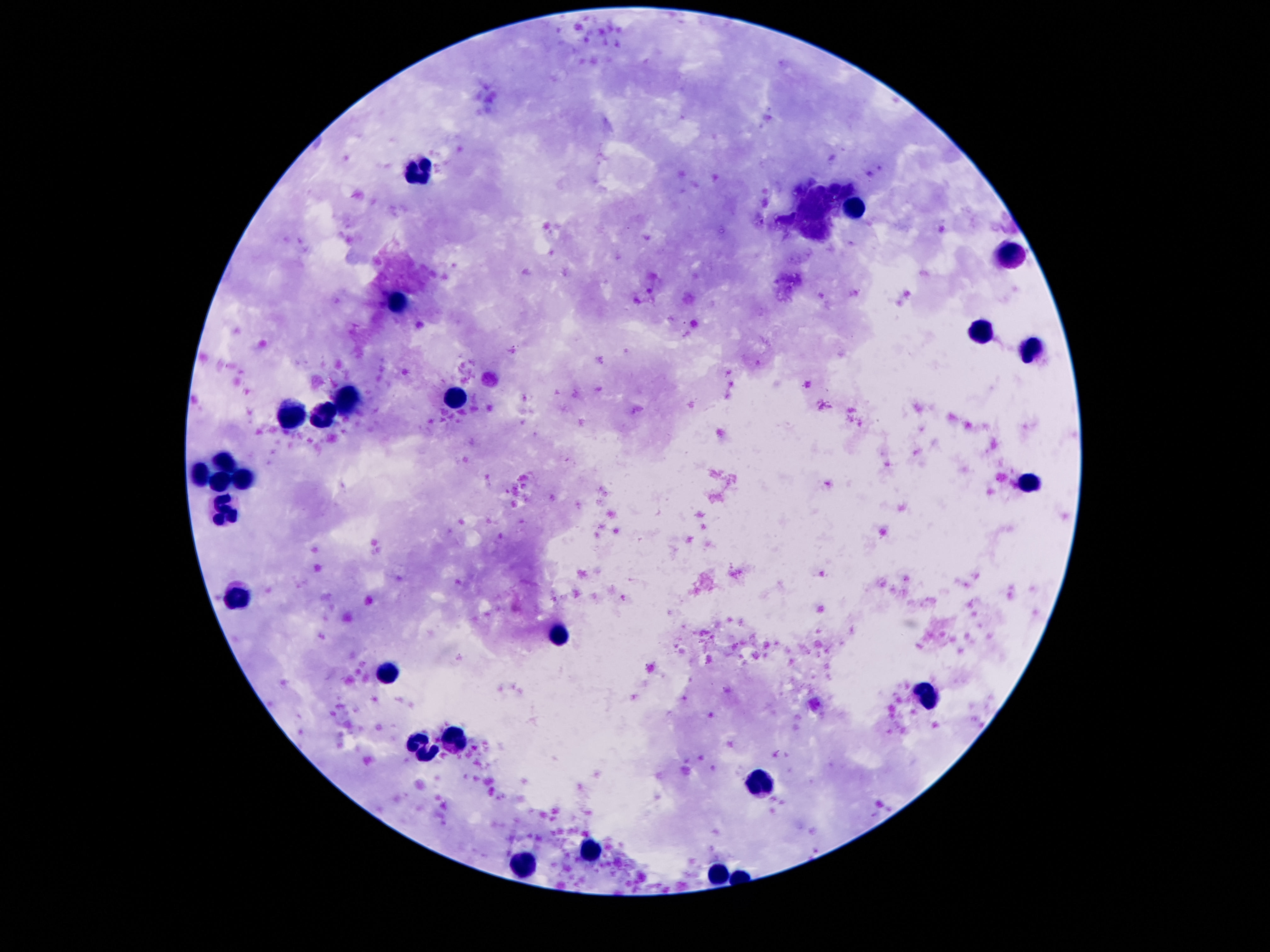

Approximate centers as {x, y} in pixels. Leukocyte locations: {422, 171}, {856, 208}, {1006, 255}, {398, 300}, {982, 330}, {1030, 351}, {458, 395}, {347, 397}, {290, 416}, {323, 416}, {228, 460}, {199, 474}, {221, 477}, {241, 479}, {1030, 485}, {226, 510}, {239, 593}, {559, 633}, {391, 673}, {927, 695}, {456, 738}, {422, 745}, {758, 785}, {593, 852}, {523, 866}, {716, 873}. 100x magnification. Photographed through the microscope eyepiece with a smartphone camera. Image is 1270×952 pixels. Giemsa stain. Patient malaria status: not infected. Thick peripheral-blood smear. Single field of view.